Give the position of every Plasmodium parasite.
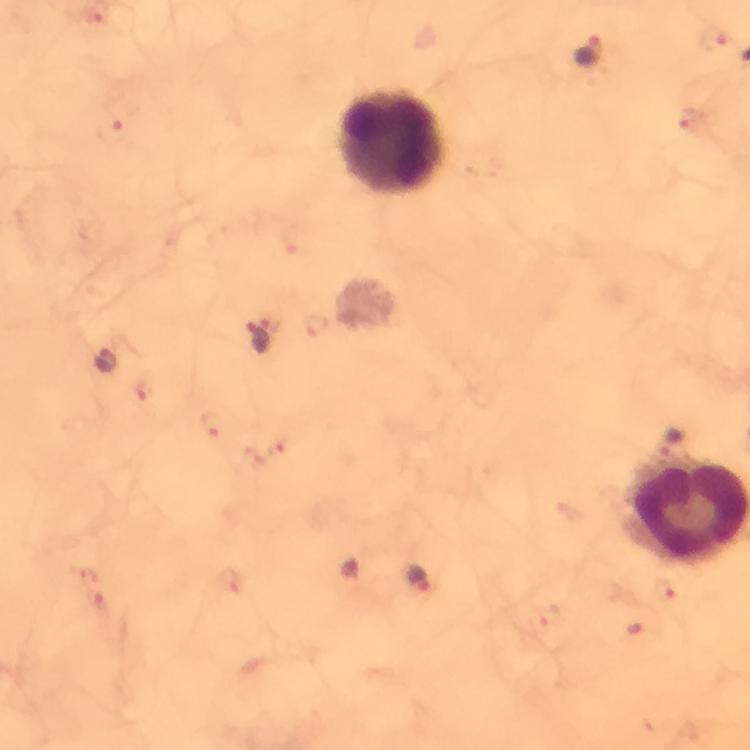

Approximate centers as [x, y] in pixels.
Plasmodium parasites: [589, 51], [259, 338], [105, 362], [671, 444], [421, 580].

Leukocyte locations: [393, 147]. Thick blood film. Image is 750×750 pixels. At 100x magnification. Cropped region of a single field of view. Immersion oil was used. Photographed through the microscope with a smartphone camera. Giemsa stain. From a malaria diagnostic workup.